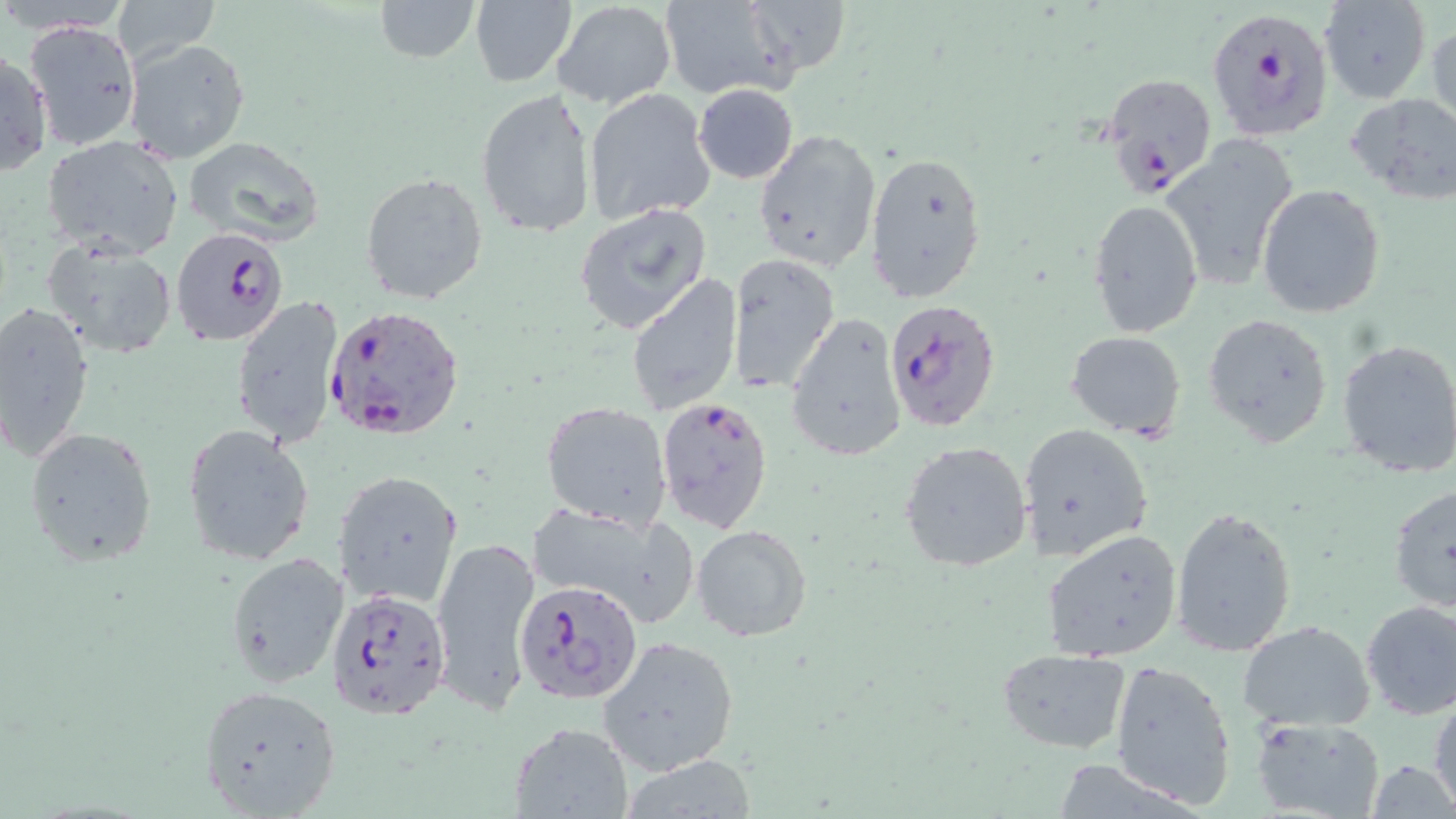

slide_level_diagnosis: Plasmodium falciparum
image_size: 1456×819 pixels
plasmodium_falciparum_infected_red_blood_cell_locations: 'approximate bounding boxes as [x1, y1, x2, y2] in pixels: [1204, 4, 1336, 144], [1099, 70, 1217, 199], [170, 227, 289, 347], [882, 298, 1002, 434], [324, 303, 466, 442], [654, 397, 773, 534], [514, 578, 643, 706], [326, 587, 452, 720]'
field_of_view: one of a larger specimen
modality: optical microscopy
preparation: thin blood film
stain: May-Grünwald-Giemsa
uninfected_red_blood_cell_locations: 'approximate bounding boxes as [x1, y1, x2, y2] in pixels: [114, 0, 221, 65], [660, 0, 792, 100], [744, 0, 851, 76], [1318, 0, 1431, 103], [373, 1, 481, 63], [468, 1, 576, 86], [552, 1, 676, 111], [24, 19, 142, 151], [1428, 21, 1456, 132], [124, 37, 251, 163], [0, 47, 51, 179], [693, 84, 800, 184], [584, 87, 717, 227], [475, 88, 597, 239], [1344, 93, 1456, 203], [753, 129, 882, 272], [43, 135, 185, 259], [184, 137, 325, 244], [1153, 138, 1292, 295], [864, 150, 987, 304], [361, 173, 489, 305], [1257, 184, 1386, 318], [1089, 199, 1203, 337], [574, 202, 713, 335], [41, 237, 178, 360], [728, 252, 841, 393], [627, 273, 743, 416], [229, 295, 343, 449], [0, 303, 96, 459], [784, 310, 909, 461], [1201, 314, 1334, 446], [1065, 331, 1186, 440], [1335, 338, 1456, 478], [541, 400, 673, 529], [1020, 422, 1154, 562], [180, 424, 316, 567], [25, 426, 157, 567], [900, 439, 1033, 575], [333, 468, 464, 610], [1387, 483, 1456, 615], [524, 502, 697, 625], [1170, 506, 1297, 659], [691, 524, 812, 642], [1044, 528, 1184, 661], [430, 536, 540, 714], [224, 552, 350, 690], [1359, 600, 1456, 720], [1237, 620, 1377, 733], [598, 635, 741, 777], [996, 648, 1134, 752], [1110, 659, 1238, 810], [197, 685, 344, 816], [1430, 693, 1456, 810], [1251, 716, 1385, 819], [508, 721, 633, 818], [616, 754, 759, 818], [1366, 760, 1454, 817]'
magnification: 1000x